Report the malaria status of this cell.
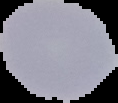

Uninfected.

Summary:
  - Image size: 118×103 pixels
  - Image type: cell region segmented out of the field of view; surrounding area masked to black
  - Preparation: thin blood smear